Report the malaria status of this cell.
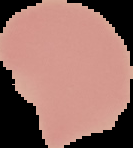
It is uninfected.

From a thin blood smear. The area outside the segmented cell region is set to black. Image is 133×148 pixels.